Name the cell type shown.
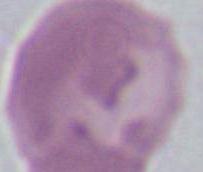
An erythrocyte.

1000x magnification. Photomicrograph.